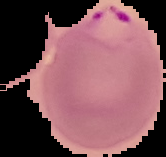
{
  "preparation": "thin blood smear",
  "result": "Plasmodium parasites identified",
  "image_type": "segmented cell region with the area outside set to black",
  "image_size": "166×157 pixels"
}